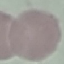

Summary:
  - Malaria status: uninfected
  - Stain: Giemsa
  - Capture: smartphone through the microscope eyepiece
  - Preparation: thin smear
  - Image type: automatically extracted cell patch, resized to 64 × 64 pixels